Comment on the morphology of the red blood cells.
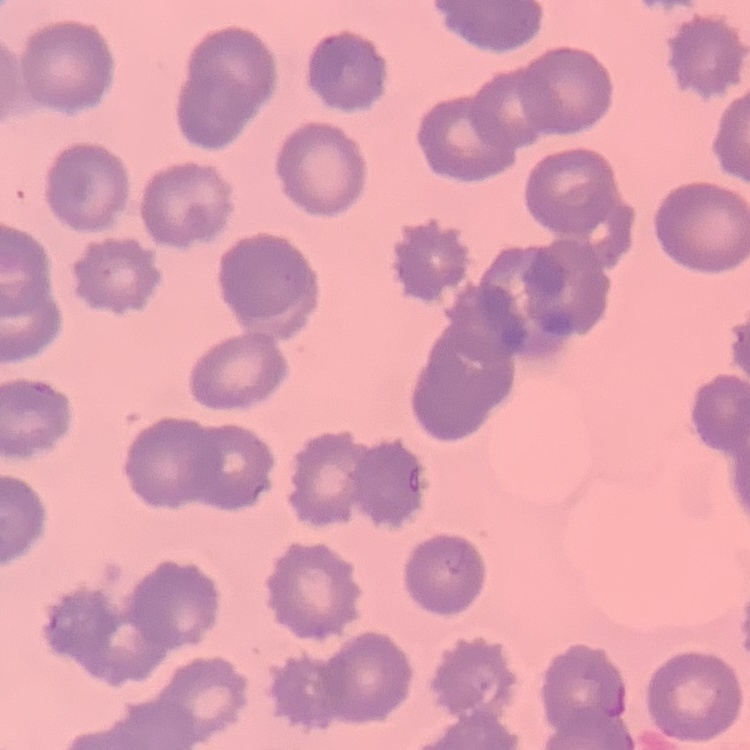
They show no rouleaux formation.

Summary:
  - Stain: Field's or Giemsa
  - Preparation: thin peripheral smear
  - Image type: square crop of a larger photomicrograph